Name the parasite shown.
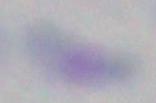

Toxoplasma gondii.

Summary:
  - Magnification: 1000x
  - Modality: photomicrograph